Assess for parasitized red blood cells.
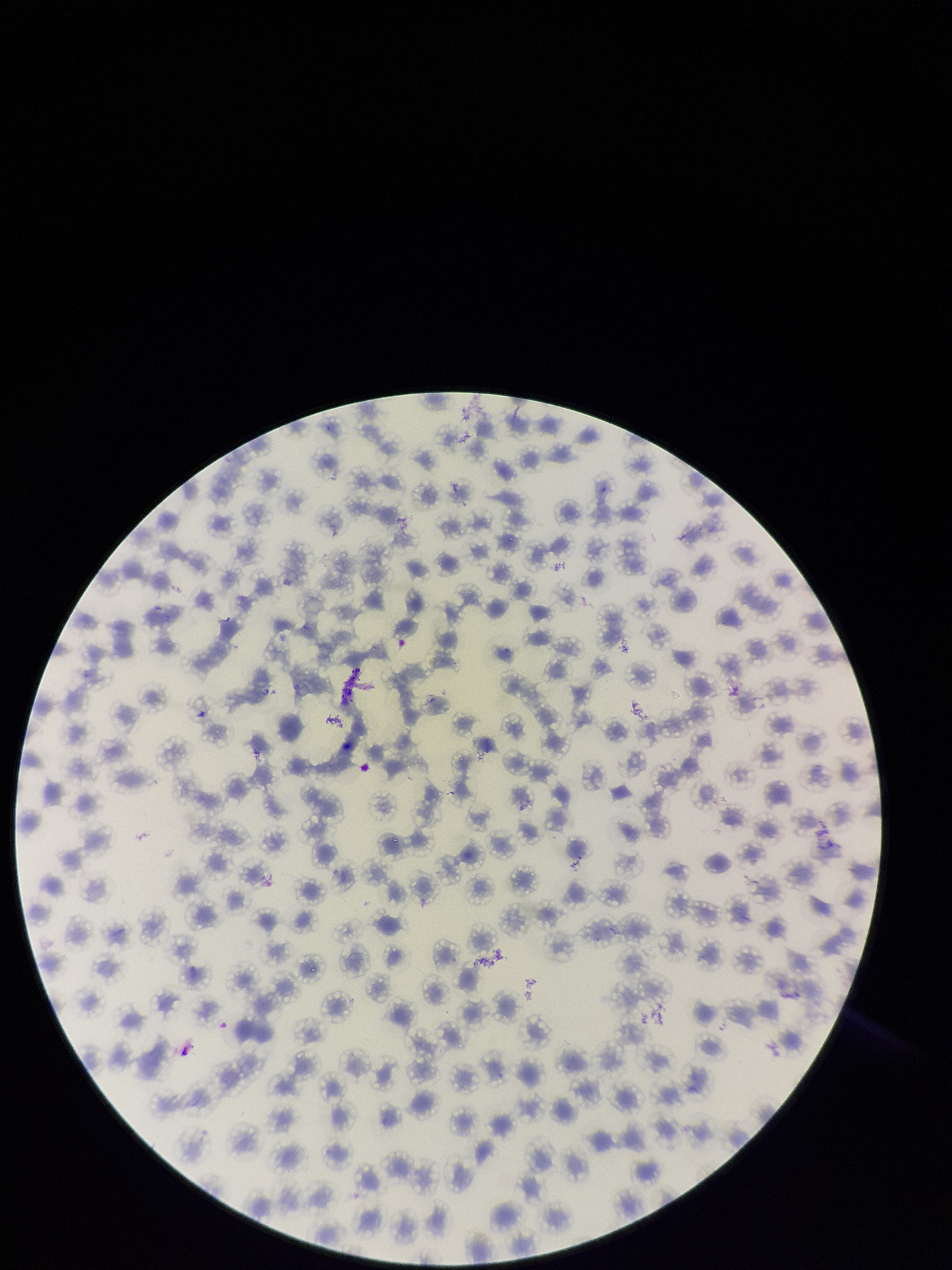
None detected.

Species reported for this patient: Plasmodium falciparum. Image is 952×1270 pixels. Preparation: thin smear. Stained with Giemsa. Parasitized red blood cell count: 0. Patient malaria status: positive. Smartphone photograph taken through the eyepiece of a microscope. Single field of view. Red blood cell count: 148.